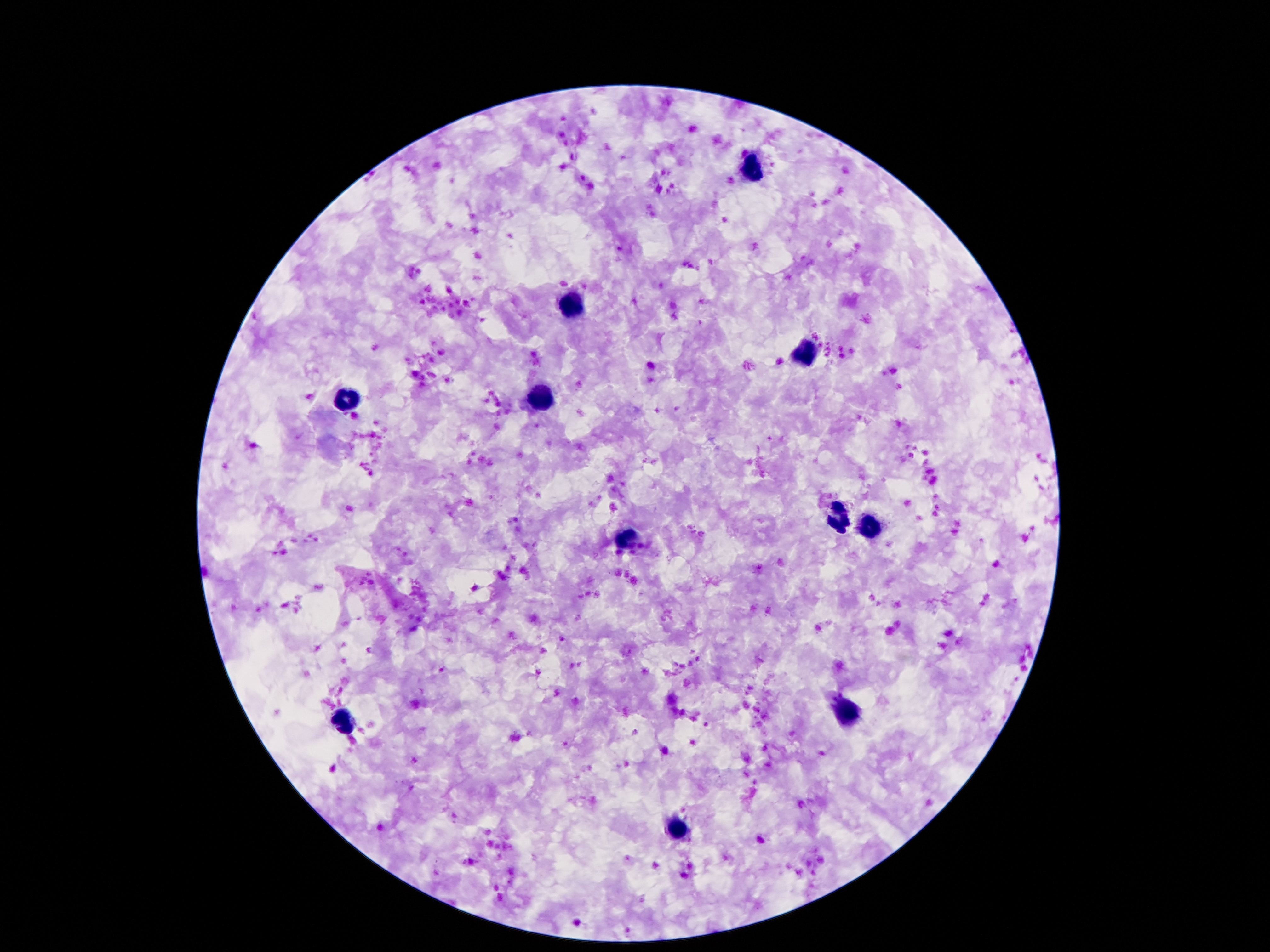 Approximate object centers, in pixels from the top-left corner. Leukocyte locations: (x=751, y=171), (x=575, y=307), (x=807, y=352), (x=344, y=397), (x=538, y=399), (x=840, y=513), (x=872, y=528), (x=624, y=542), (x=848, y=715), (x=344, y=720), (x=680, y=829). Thick blood film. 100x magnification. Patient malaria status: not infected. Giemsa stain. Image is 1270×952 pixels. Single field of view. Smartphone photograph taken through the microscope eyepiece.